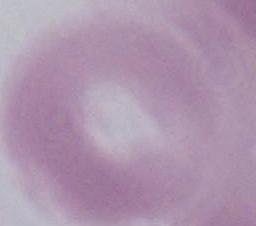
Summary:
  - Identification: red blood cell
  - Modality: micrograph
  - Magnification: 1000x